Classify this cell by malaria status.
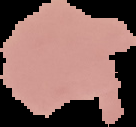

Uninfected.

Summary:
  - Preparation: thin blood film
  - Image size: 136×127 pixels
  - Image type: segmented cell region on a black background